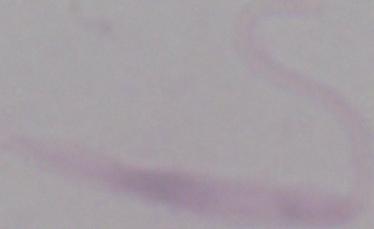

A Leishmania parasite is seen. Captured at 1000x magnification. Photomicrograph.